Classify this cell by malaria status.
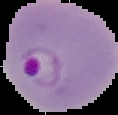
It is parasitized.

From a thin blood smear. Cell region segmented out of the field of view; the surrounding area is masked to black. Image is 118×115 pixels.